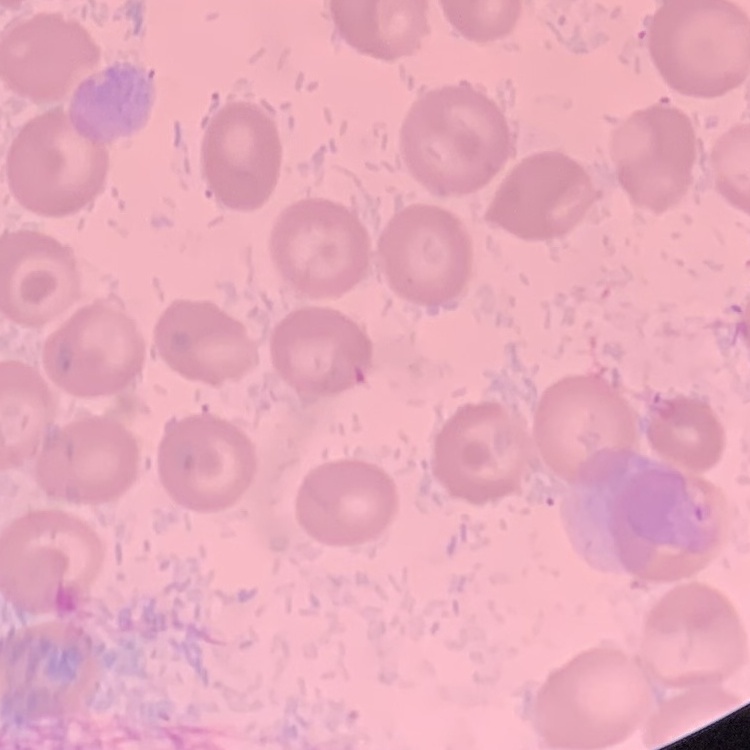
erythrocyte_morphology: no rouleaux formation
preparation: thin peripheral smear
stain: Field's or Giemsa
image_type: one tile cut from a larger photomicrograph